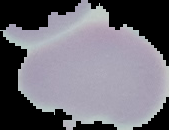

Malaria status: uninfected. Cell region segmented out of the field of view; the surrounding area is masked to black. From a thin blood film. Image is 169×130 pixels.